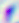
Toxoplasma gondii is seen. Micrograph. Captured at 400x magnification.